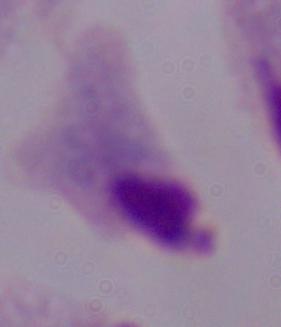
modality = micrograph
magnification = 1000x
identification = trichomonad